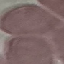
malaria status = uninfected
image type = cell patch, automatically extracted from a larger field of view and resized to 64 × 64 pixels
stain = Giemsa
capture = smartphone through the microscope eyepiece
preparation = thin smear